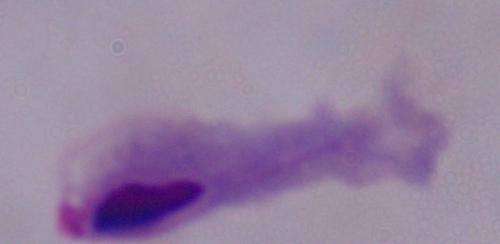
identification = trichomonad
magnification = 1000x
modality = micrograph